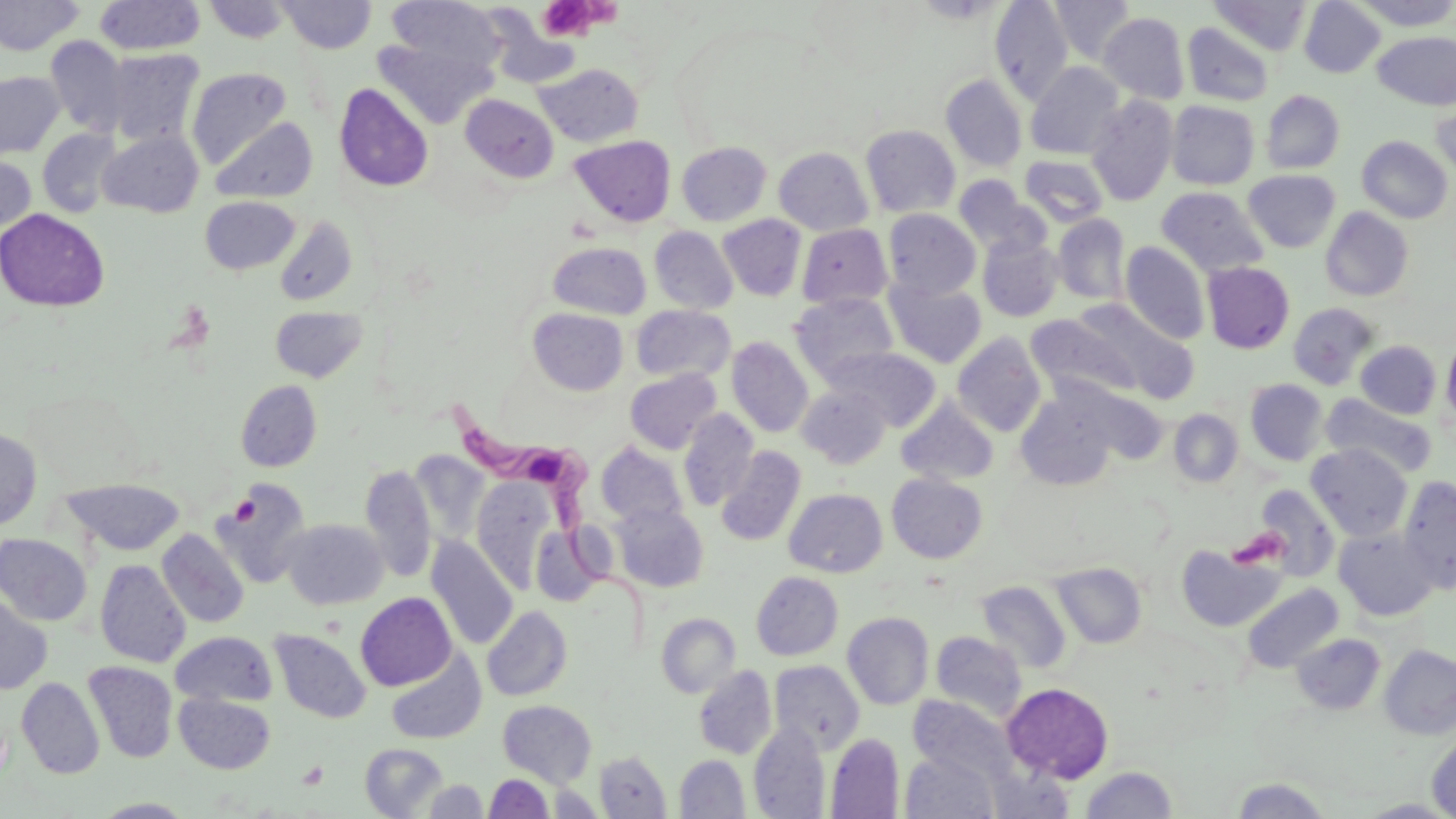
{
  "slide_level_diagnosis": "Trypanosoma brucei",
  "field_of_view": "single",
  "image_size": "1456×819 pixels",
  "trypanosoma_brucei_locations": "approximate bounding boxes as named x1/y1/x2/y2 corners in pixels: (x1=446, y1=397, x2=662, y2=656)",
  "stain": "May-Grünwald-Giemsa",
  "modality": "light microscopy",
  "magnification": "1000x",
  "uninfected_red_blood_cell_locations": "approximate bounding boxes as named x1/y1/x2/y2 corners in pixels: (x1=0, y1=0, x2=84, y2=56), (x1=95, y1=0, x2=205, y2=56), (x1=202, y1=0, x2=292, y2=43), (x1=385, y1=0, x2=505, y2=78), (x1=990, y1=0, x2=1074, y2=105), (x1=1050, y1=0, x2=1137, y2=65), (x1=1299, y1=0, x2=1385, y2=78), (x1=1353, y1=0, x2=1456, y2=30), (x1=277, y1=1, x2=377, y2=53), (x1=1210, y1=1, x2=1312, y2=56), (x1=481, y1=7, x2=581, y2=89), (x1=1098, y1=11, x2=1189, y2=104), (x1=1182, y1=23, x2=1275, y2=107), (x1=1373, y1=31, x2=1456, y2=110), (x1=44, y1=35, x2=129, y2=137), (x1=374, y1=36, x2=495, y2=130), (x1=104, y1=47, x2=205, y2=147), (x1=1025, y1=62, x2=1126, y2=160), (x1=533, y1=63, x2=643, y2=147), (x1=186, y1=68, x2=292, y2=167), (x1=0, y1=71, x2=65, y2=158), (x1=940, y1=74, x2=1028, y2=172), (x1=334, y1=83, x2=434, y2=192), (x1=1260, y1=90, x2=1345, y2=174), (x1=461, y1=94, x2=558, y2=183), (x1=1086, y1=94, x2=1179, y2=207), (x1=1431, y1=94, x2=1455, y2=184), (x1=1166, y1=100, x2=1259, y2=189), (x1=210, y1=117, x2=317, y2=203), (x1=860, y1=125, x2=960, y2=218), (x1=37, y1=128, x2=122, y2=217), (x1=98, y1=131, x2=203, y2=217), (x1=569, y1=135, x2=676, y2=227), (x1=1357, y1=135, x2=1452, y2=223), (x1=676, y1=142, x2=771, y2=226), (x1=774, y1=147, x2=873, y2=236), (x1=1019, y1=154, x2=1109, y2=227), (x1=0, y1=155, x2=36, y2=234), (x1=1243, y1=169, x2=1341, y2=253), (x1=954, y1=175, x2=1047, y2=256), (x1=1156, y1=186, x2=1268, y2=276), (x1=200, y1=196, x2=300, y2=275), (x1=1321, y1=207, x2=1414, y2=301), (x1=0, y1=208, x2=110, y2=312), (x1=883, y1=209, x2=981, y2=300), (x1=717, y1=214, x2=806, y2=301), (x1=1052, y1=214, x2=1131, y2=304), (x1=274, y1=216, x2=359, y2=306), (x1=797, y1=223, x2=892, y2=310), (x1=649, y1=225, x2=738, y2=315), (x1=977, y1=235, x2=1062, y2=322), (x1=548, y1=241, x2=651, y2=319), (x1=1121, y1=242, x2=1210, y2=344), (x1=1202, y1=261, x2=1295, y2=353), (x1=886, y1=279, x2=986, y2=368), (x1=791, y1=293, x2=899, y2=382), (x1=1288, y1=302, x2=1380, y2=390), (x1=1074, y1=303, x2=1200, y2=405), (x1=631, y1=305, x2=735, y2=382), (x1=270, y1=306, x2=367, y2=382), (x1=528, y1=308, x2=629, y2=395), (x1=1026, y1=313, x2=1139, y2=405), (x1=952, y1=332, x2=1047, y2=437), (x1=1441, y1=332, x2=1456, y2=430), (x1=726, y1=336, x2=814, y2=437), (x1=1356, y1=340, x2=1441, y2=419), (x1=827, y1=347, x2=941, y2=431), (x1=625, y1=368, x2=722, y2=454), (x1=1245, y1=379, x2=1328, y2=465), (x1=236, y1=380, x2=322, y2=471), (x1=797, y1=384, x2=892, y2=468), (x1=1014, y1=389, x2=1121, y2=491), (x1=1321, y1=394, x2=1438, y2=479), (x1=896, y1=397, x2=999, y2=486), (x1=678, y1=409, x2=759, y2=511), (x1=1169, y1=409, x2=1243, y2=488), (x1=0, y1=428, x2=42, y2=531), (x1=597, y1=442, x2=689, y2=528), (x1=1306, y1=444, x2=1412, y2=541), (x1=716, y1=446, x2=806, y2=546), (x1=409, y1=451, x2=490, y2=544), (x1=360, y1=464, x2=437, y2=581), (x1=887, y1=473, x2=987, y2=563), (x1=1397, y1=475, x2=1456, y2=593), (x1=60, y1=478, x2=184, y2=556), (x1=472, y1=478, x2=553, y2=590), (x1=212, y1=482, x2=312, y2=588), (x1=1253, y1=485, x2=1340, y2=582), (x1=784, y1=488, x2=888, y2=577), (x1=612, y1=505, x2=709, y2=592), (x1=282, y1=519, x2=388, y2=609), (x1=530, y1=526, x2=603, y2=606), (x1=1334, y1=528, x2=1438, y2=621), (x1=157, y1=529, x2=249, y2=627), (x1=0, y1=534, x2=92, y2=625), (x1=427, y1=537, x2=519, y2=649), (x1=1176, y1=543, x2=1285, y2=632), (x1=95, y1=560, x2=191, y2=668), (x1=1051, y1=562, x2=1147, y2=648), (x1=751, y1=571, x2=843, y2=660), (x1=976, y1=580, x2=1072, y2=674), (x1=1241, y1=583, x2=1344, y2=674), (x1=355, y1=592, x2=456, y2=691), (x1=0, y1=595, x2=53, y2=694), (x1=482, y1=606, x2=572, y2=701), (x1=842, y1=612, x2=933, y2=710), (x1=656, y1=613, x2=741, y2=698), (x1=270, y1=629, x2=370, y2=723), (x1=171, y1=632, x2=277, y2=707), (x1=931, y1=632, x2=1026, y2=721), (x1=1291, y1=633, x2=1385, y2=715), (x1=1379, y1=645, x2=1456, y2=740), (x1=385, y1=650, x2=487, y2=745), (x1=83, y1=661, x2=178, y2=763), (x1=769, y1=661, x2=865, y2=753), (x1=694, y1=665, x2=776, y2=759), (x1=16, y1=677, x2=105, y2=779), (x1=1002, y1=682, x2=1114, y2=783), (x1=175, y1=693, x2=275, y2=774), (x1=909, y1=695, x2=1013, y2=784), (x1=498, y1=700, x2=597, y2=787), (x1=749, y1=722, x2=830, y2=818), (x1=825, y1=733, x2=904, y2=818), (x1=1427, y1=733, x2=1456, y2=819), (x1=360, y1=742, x2=448, y2=818), (x1=595, y1=751, x2=670, y2=818), (x1=901, y1=751, x2=999, y2=818), (x1=675, y1=755, x2=750, y2=818), (x1=988, y1=766, x2=1076, y2=818), (x1=1079, y1=767, x2=1178, y2=817), (x1=484, y1=774, x2=554, y2=818), (x1=1229, y1=777, x2=1332, y2=818), (x1=423, y1=779, x2=488, y2=818), (x1=92, y1=798, x2=198, y2=818)",
  "platelet_locations": "approximate bounding boxes as named x1/y1/x2/y2 corners in pixels: (x1=537, y1=0, x2=597, y2=40), (x1=227, y1=490, x2=283, y2=543), (x1=230, y1=495, x2=260, y2=527), (x1=1226, y1=528, x2=1288, y2=570)",
  "preparation": "thin blood film"
}